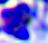

Summary:
  - Magnification: 400x
  - Identification: white blood cell
  - Modality: photomicrograph